Identify the parasite.
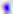

Toxoplasma gondii.

Summary:
  - Magnification: 400x
  - Modality: photomicrograph